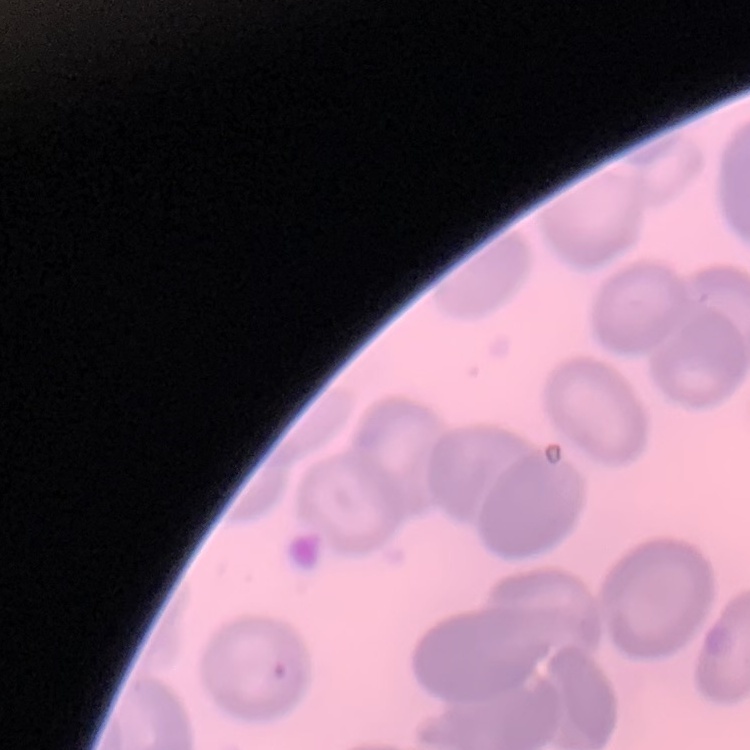

Summary:
  - Red blood cell morphology: no rouleaux formation
  - Stain: Field's or Giemsa
  - Preparation: thin blood film
  - Image type: one tile cut from a larger photomicrograph